Name the cell type shown.
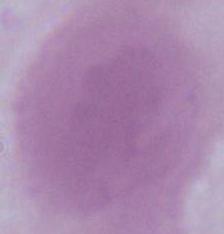
This is an erythrocyte.

magnification = 1000x
modality = photomicrograph